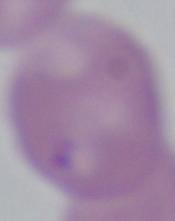

Summary:
  - Modality: photomicrograph
  - Magnification: 1000x
  - Identification: Babesia